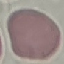

Summary:
  - Malaria status: uninfected
  - Stain: Giemsa
  - Preparation: thin smear
  - Image type: cell patch, automatically extracted from a larger field of view and resized to 64 × 64 pixels
  - Capture: smartphone through the microscope eyepiece